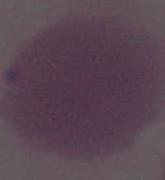
Micrograph. Captured at 1000x magnification. An erythrocyte is seen.